Outline each uninfected red blood cell.
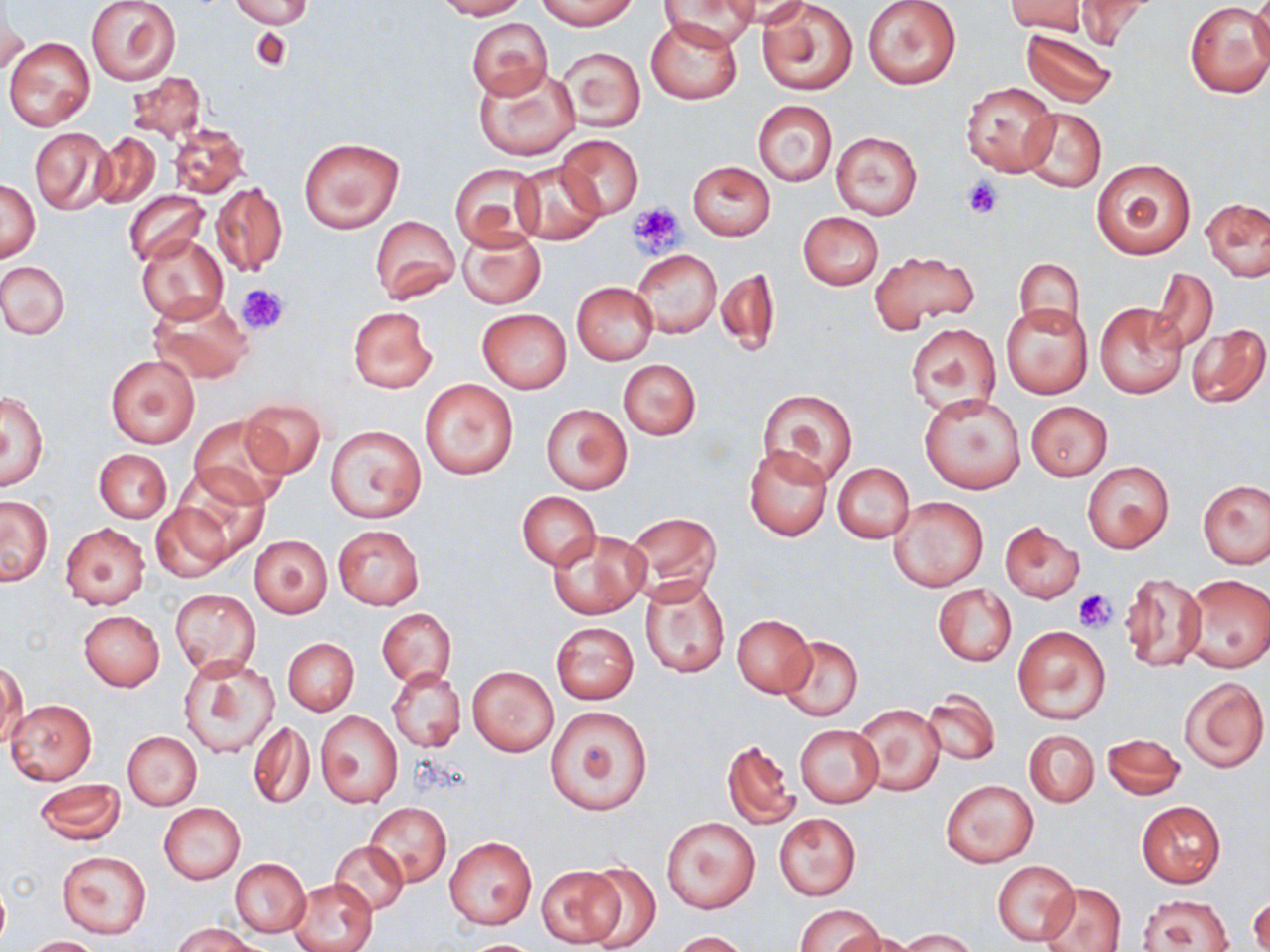

Approximate bounding boxes as [x1, y1, x2, y2] in pixels.
Uninfected red blood cells: [228, 0, 315, 29], [436, 0, 527, 19], [538, 0, 637, 30], [658, 0, 761, 50], [719, 0, 814, 28], [862, 0, 963, 89], [1008, 0, 1091, 36], [1249, 0, 1270, 75], [85, 1, 181, 87], [759, 1, 858, 97], [1069, 1, 1158, 49], [1182, 1, 1270, 98], [1, 2, 28, 76], [646, 16, 742, 104], [467, 18, 551, 100], [1019, 27, 1117, 106], [5, 37, 94, 130], [555, 46, 645, 133], [476, 66, 582, 160], [125, 72, 208, 142], [961, 82, 1059, 177], [753, 101, 837, 185], [1017, 107, 1106, 194], [168, 122, 249, 198], [29, 127, 114, 216], [831, 131, 922, 220], [91, 132, 159, 209], [557, 136, 643, 220], [298, 138, 404, 234], [1092, 158, 1196, 259], [512, 160, 604, 245], [688, 160, 775, 240], [451, 163, 544, 248], [1, 180, 40, 263], [210, 181, 289, 278], [124, 190, 208, 268], [1202, 197, 1270, 281], [798, 212, 883, 290], [370, 215, 459, 301], [457, 228, 547, 310], [135, 234, 228, 322], [631, 249, 721, 339], [867, 249, 980, 332], [1014, 258, 1084, 336], [1, 260, 69, 339], [715, 266, 782, 359], [1150, 269, 1218, 353], [572, 282, 658, 363], [148, 293, 252, 383], [1095, 302, 1189, 398], [1002, 304, 1093, 398], [348, 306, 436, 392], [477, 308, 571, 392], [906, 322, 1000, 418], [1185, 322, 1268, 409], [105, 355, 199, 448], [618, 359, 700, 440], [419, 378, 520, 481], [757, 387, 857, 487], [2, 388, 50, 492], [919, 393, 1026, 493], [238, 397, 327, 478], [1025, 401, 1113, 481], [542, 403, 631, 495], [190, 416, 290, 507], [325, 426, 426, 523], [744, 445, 833, 541], [93, 449, 170, 522], [1082, 461, 1175, 553], [832, 463, 915, 543], [164, 473, 268, 566], [1199, 478, 1270, 569], [518, 492, 600, 569], [891, 496, 988, 591], [1, 497, 52, 585], [151, 499, 238, 582], [623, 512, 722, 601], [60, 523, 150, 610], [999, 523, 1084, 603], [332, 525, 425, 610], [546, 530, 650, 619], [249, 534, 333, 618], [1120, 573, 1207, 672], [1181, 574, 1270, 672], [640, 575, 732, 679], [932, 584, 1016, 666], [169, 587, 260, 678], [378, 608, 454, 688], [79, 610, 164, 691], [732, 614, 815, 697], [549, 621, 640, 704], [1011, 624, 1111, 725], [777, 635, 863, 721], [283, 638, 359, 715], [179, 657, 280, 757], [0, 661, 27, 750], [467, 666, 558, 756], [388, 668, 466, 752], [1179, 676, 1268, 772], [921, 690, 1001, 765], [7, 700, 96, 785], [853, 703, 944, 796], [545, 706, 653, 815], [316, 711, 402, 807], [248, 721, 314, 809], [795, 724, 883, 806], [1023, 730, 1099, 807], [122, 731, 203, 810], [1102, 732, 1185, 800], [722, 738, 798, 830], [33, 779, 125, 845], [941, 780, 1037, 866], [1136, 800, 1225, 888], [159, 803, 246, 884], [364, 803, 452, 887], [773, 811, 860, 901], [661, 816, 759, 913], [444, 836, 536, 929], [330, 840, 409, 913], [57, 850, 152, 938], [230, 858, 310, 937], [992, 860, 1079, 945], [582, 862, 662, 948], [537, 867, 624, 947], [289, 877, 376, 952], [0, 879, 10, 951], [1042, 883, 1124, 951], [1249, 894, 1270, 952], [1137, 895, 1234, 951], [794, 903, 883, 952], [174, 922, 259, 952], [899, 929, 979, 952], [669, 931, 751, 951], [840, 931, 916, 952], [22, 935, 104, 952], [461, 938, 547, 951].

slide_level_diagnosis: negative for blood parasites
image_size: 1270×952 pixels
stain: May-Grünwald-Giemsa
platelet_locations: 'approximate bounding boxes as [x1, y1, x2, y2] in pixels: [961, 177, 1003, 218], [627, 202, 684, 258], [236, 283, 289, 336], [1073, 587, 1116, 633]'
magnification: 1000x
modality: light microscopy
field_of_view: one of a larger specimen
preparation: thin blood smear